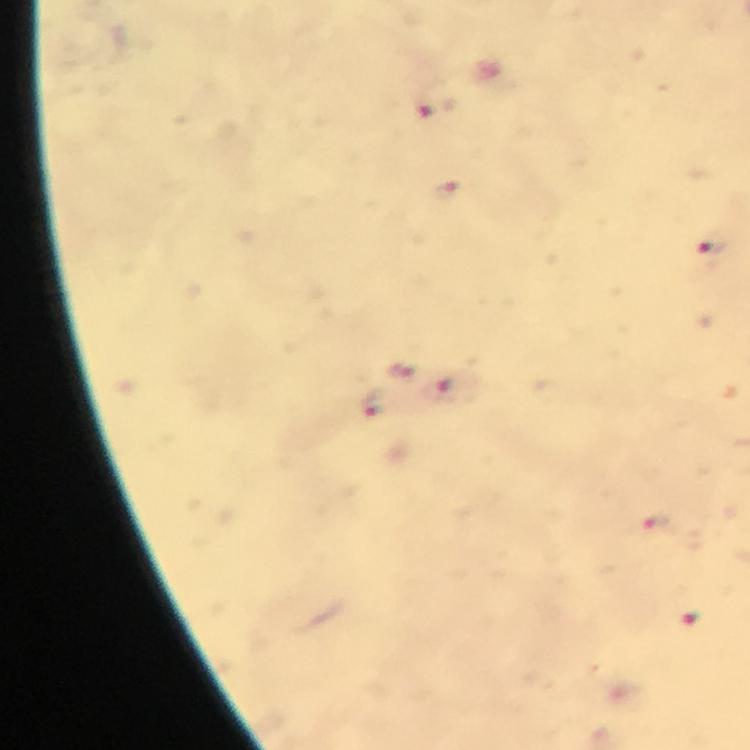

{
  "cropped_from": "one field of view",
  "context": "from a malaria diagnostic workup",
  "stain": "Giemsa",
  "capture": "smartphone mounted on the microscope",
  "malaria_parasite_locations": "approximate centers as (x, y) in pixels: (426, 104), (710, 249), (399, 368), (450, 391), (373, 404), (653, 525), (688, 621)",
  "magnification": "100x",
  "preparation": "thick blood film",
  "immersion_oil": "used",
  "image_size": "750×750 pixels"
}